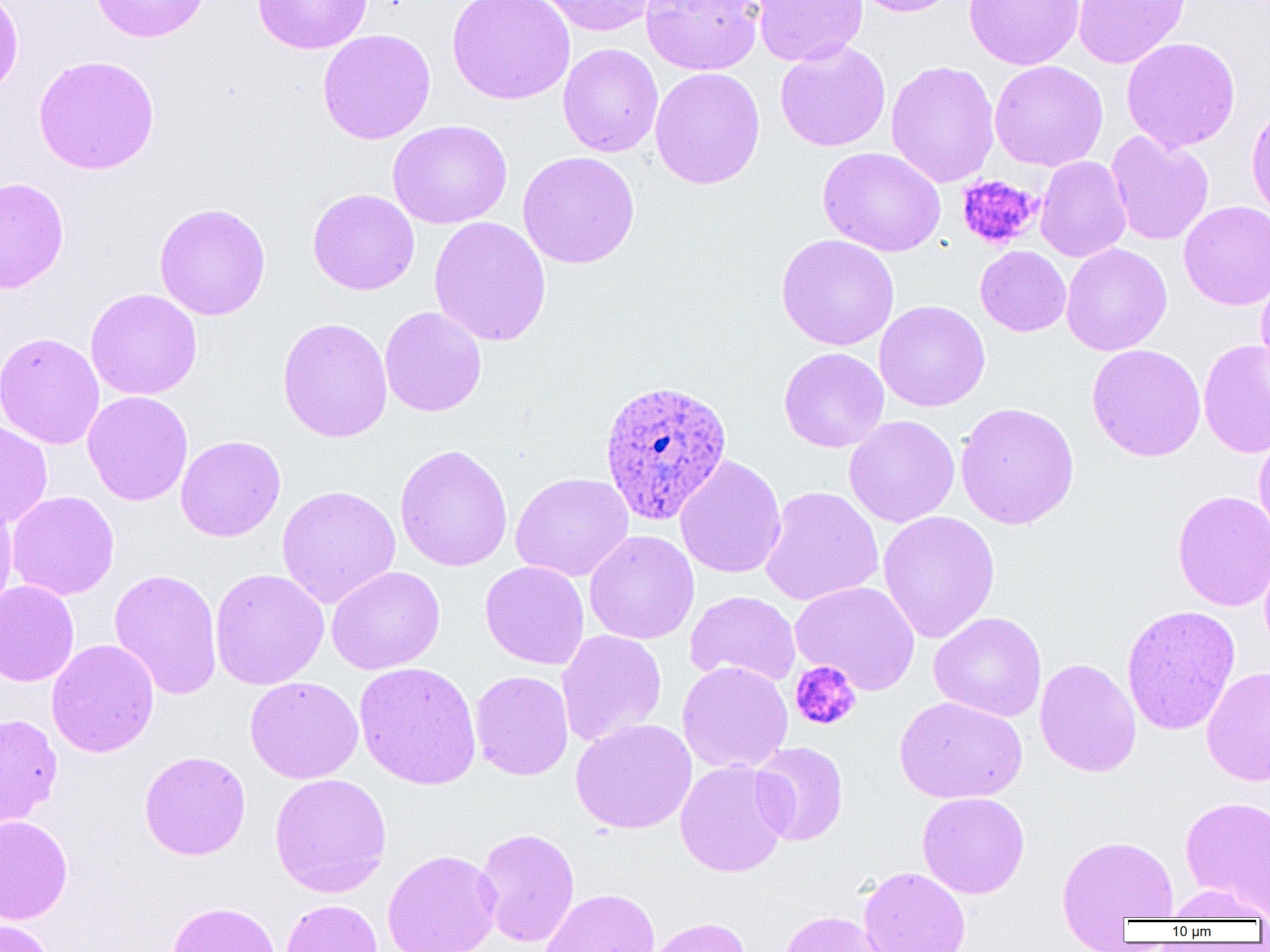 Approximate bounding boxes as (x1,y1)-(x2,y2) corner pairs in pixels. Plasmodium ovale-infected red blood cell locations: (599,378)-(732,524). Platelet locations: (956,175)-(1042,250), (790,661)-(862,731). Uninfected red blood cell locations: (0,0)-(23,99), (91,0)-(209,43), (253,0)-(373,54), (447,0)-(575,105), (537,0)-(661,36), (641,0)-(764,75), (752,0)-(868,66), (850,0)-(963,17), (963,0)-(1085,70), (1072,0)-(1190,69), (317,29)-(436,145), (1121,37)-(1241,153), (775,40)-(891,152), (558,43)-(663,157), (33,54)-(160,175), (885,59)-(1000,188), (989,60)-(1108,171), (649,67)-(765,190), (1246,101)-(1270,222), (387,119)-(512,229), (1106,131)-(1215,246), (817,146)-(947,256), (517,151)-(640,269), (1034,155)-(1132,262), (0,177)-(69,294), (308,188)-(420,295), (1178,200)-(1270,310), (153,202)-(271,320), (429,215)-(552,346), (776,234)-(899,351), (1061,243)-(1172,356), (975,246)-(1071,336), (1255,269)-(1270,388), (85,288)-(202,400), (874,300)-(990,412), (379,307)-(487,417), (277,317)-(393,442), (0,331)-(105,450), (1198,339)-(1270,458), (1086,343)-(1206,462), (779,347)-(889,453), (82,391)-(193,506), (955,401)-(1080,529), (844,415)-(960,528), (0,419)-(53,529), (1253,425)-(1270,543), (175,435)-(286,542), (394,443)-(513,573), (675,455)-(786,579), (510,472)-(634,582), (276,485)-(401,609), (759,485)-(884,607), (6,490)-(120,600), (1172,490)-(1270,611), (0,500)-(17,615), (878,510)-(1000,644), (584,530)-(699,644), (1259,546)-(1270,658), (480,561)-(590,670), (326,565)-(445,675), (109,568)-(223,701), (209,568)-(330,690), (0,580)-(80,687), (789,581)-(920,695), (685,591)-(801,687), (1121,604)-(1240,736), (928,611)-(1047,722), (557,629)-(667,747), (46,639)-(159,758), (1034,658)-(1141,777), (677,661)-(793,774), (354,662)-(482,790), (1201,665)-(1270,786), (470,670)-(574,780), (245,676)-(363,784), (894,695)-(1027,804), (0,713)-(62,830), (570,719)-(697,834), (750,741)-(849,846), (139,750)-(251,860), (674,759)-(791,878), (269,773)-(392,898), (917,791)-(1030,899), (1179,795)-(1270,916), (0,815)-(73,924), (474,827)-(581,948), (1056,834)-(1179,933), (382,849)-(502,952), (859,866)-(972,952), (1163,883)-(1269,923), (540,888)-(660,952), (280,898)-(382,952), (166,901)-(282,952), (777,910)-(892,952), (644,916)-(752,952), (0,918)-(58,952). Slide-level diagnosis: Plasmodium ovale. Captured at 1000x magnification. Thin blood film. Image is 1270×952 pixels. Optical microscopy. Single field of view.